Name the parasite shown.
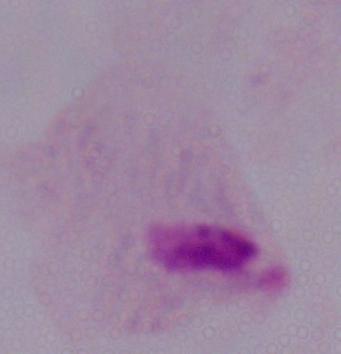
A trichomonad.

Captured at 1000x magnification. Photomicrograph.